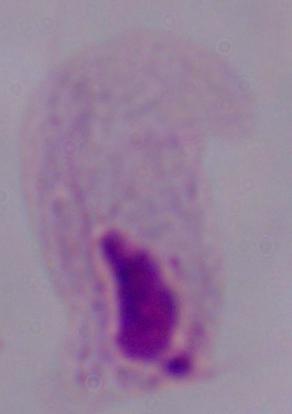
magnification = 1000x
modality = micrograph
identification = trichomonad